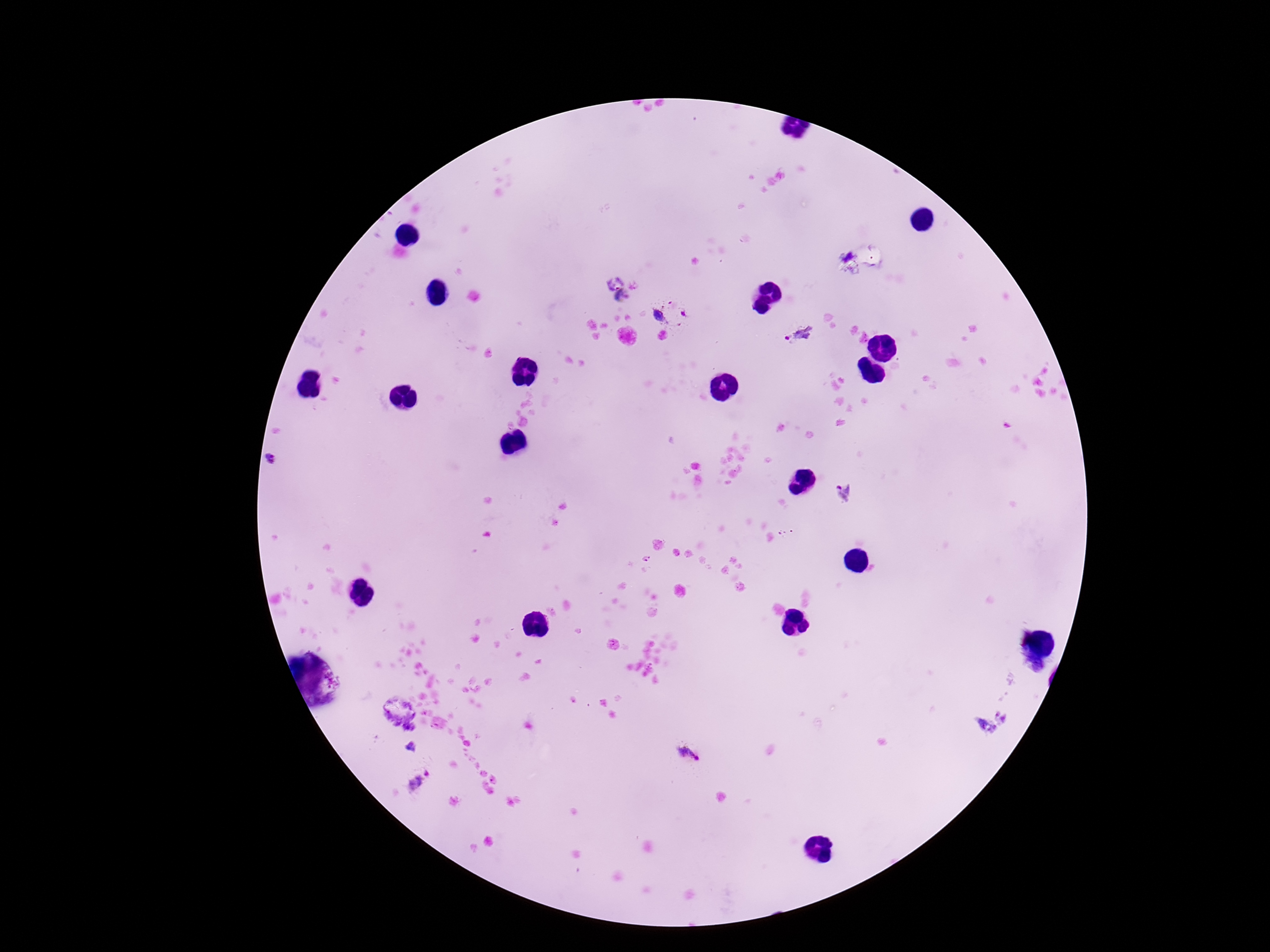
{
  "patient_malaria_status": "positive",
  "magnification": "100x",
  "plasmodium_parasite_locations": "approximate centers as (x, y) in pixels: (614, 279), (624, 298), (657, 315), (799, 335), (273, 460), (843, 495), (993, 724), (686, 755), (418, 780)",
  "stain": "Giemsa",
  "image_size": "1270×952 pixels",
  "field_of_view": "single",
  "capture": "smartphone camera through the microscope eyepiece",
  "preparation": "thick blood smear"
}